Assess this cell for malaria.
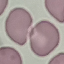
It is uninfected.

{
  "capture": "smartphone through the microscope eyepiece",
  "preparation": "thin blood smear",
  "image_type": "cell patch, automatically extracted from a larger field of view and resized to 64 × 64 pixels",
  "stain": "Giemsa"
}